Assess the morphology of the erythrocytes.
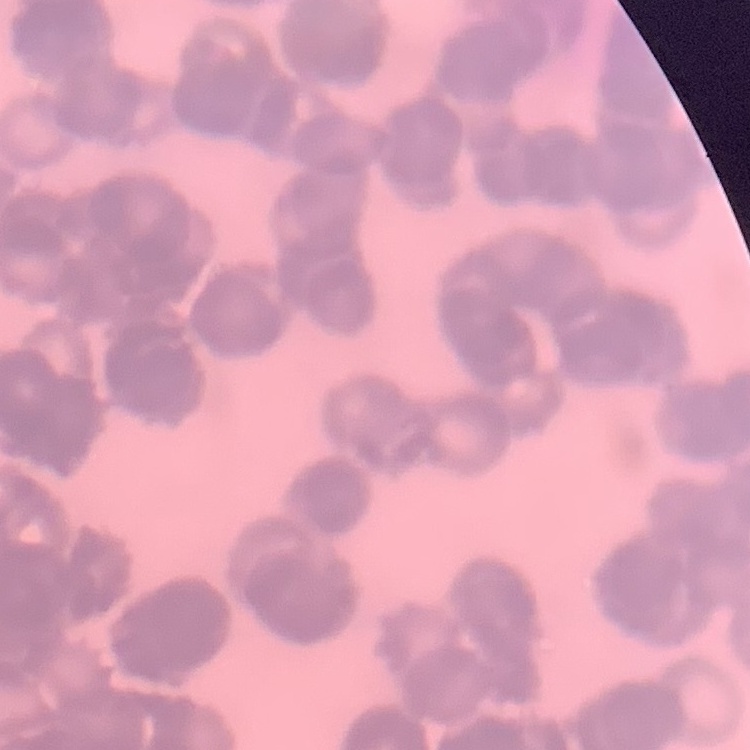
They show rouleaux formation.

preparation = thin peripheral smear
stain = Field's or Giemsa
image type = one tile cut from a larger photomicrograph